Identify the parasite.
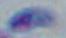
This is Toxoplasma gondii.

Summary:
  - Modality: micrograph
  - Magnification: 1000x